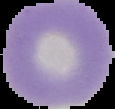
Summary:
  - Result: no Plasmodium parasites seen
  - Image size: 115×109 pixels
  - Preparation: thin blood smear
  - Image type: segmented cell region with the area outside set to black